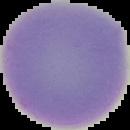
Result: negative for malaria parasites. From a thin blood film. Image is 130×130 pixels. Segmented cell region on a black background.